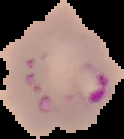

Summary:
  - Result: Plasmodium parasites detected
  - Image size: 124×139 pixels
  - Preparation: thin blood film
  - Image type: segmented cell region on a black background